Classify this cell by malaria status.
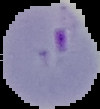
Parasitized.

{
  "image_size": "100×109 pixels",
  "image_type": "segmented cell region with the area outside set to black",
  "preparation": "thin blood smear"
}